State which parasite is depicted.
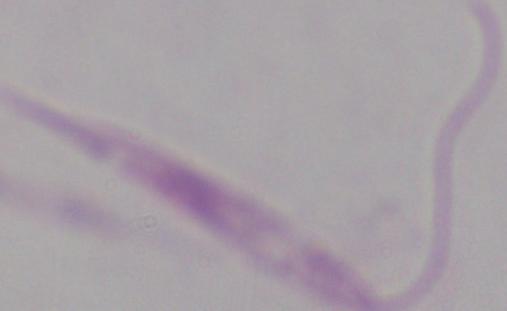

Leishmania.

Summary:
  - Modality: photomicrograph
  - Magnification: 1000x